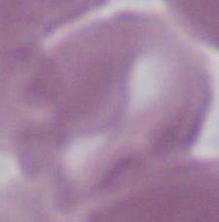

identification = red blood cell
modality = micrograph
magnification = 1000x